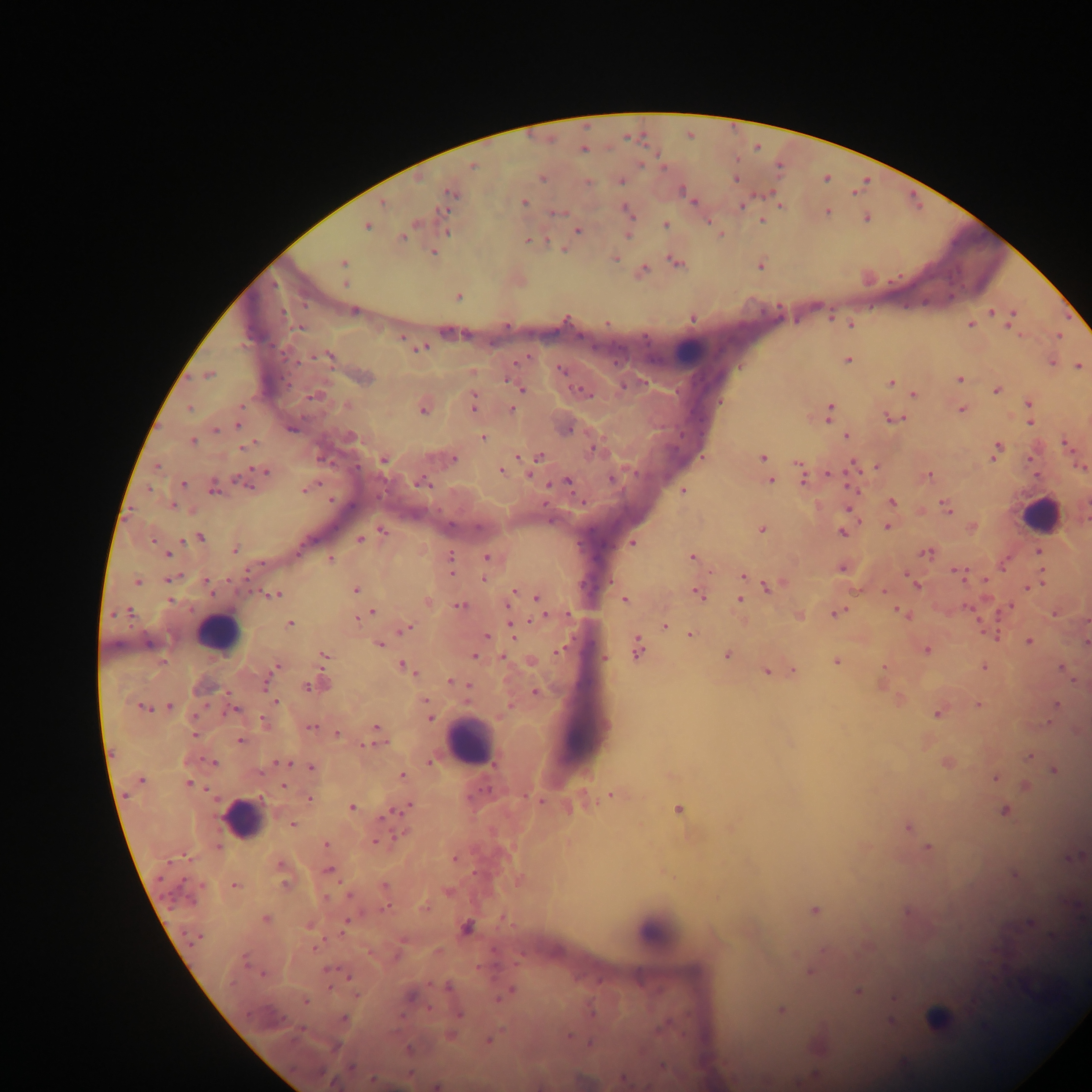
Approximate centers as [x, y] in pixels. Leukocyte locations: [692, 350], [1040, 516], [219, 634], [468, 742], [242, 819], [657, 936]. Malaria parasite locations: [583, 150], [472, 165], [543, 178], [735, 179], [620, 182], [588, 183], [450, 193], [383, 203], [524, 203], [742, 204], [780, 205], [627, 210], [557, 212], [827, 212], [867, 218], [761, 221], [415, 224], [665, 225], [367, 226], [447, 230], [578, 230], [627, 236], [403, 237], [528, 240], [434, 252], [615, 258], [343, 263], [676, 264], [760, 265], [644, 269], [346, 283], [459, 296], [353, 311], [991, 312], [1013, 315], [692, 318], [607, 322], [850, 324], [971, 324], [299, 328], [401, 337], [421, 348], [329, 356], [847, 360], [520, 361], [1051, 362], [1078, 366], [561, 369], [209, 375], [365, 378], [960, 379], [891, 382], [521, 388], [997, 390], [582, 392], [914, 394], [315, 396], [473, 403], [1029, 405], [190, 409], [512, 410], [961, 410], [423, 411], [830, 411], [894, 418], [1030, 423], [238, 425], [292, 428], [216, 430], [568, 430], [846, 436], [352, 437], [483, 438], [192, 441], [1066, 444], [246, 446], [996, 449], [594, 450], [762, 457], [454, 458], [538, 458], [384, 460], [799, 464], [158, 466], [875, 466], [853, 467], [1082, 467], [264, 471], [501, 471], [929, 475], [802, 477], [611, 478], [771, 481], [242, 482], [559, 482], [567, 482], [421, 483], [182, 484], [306, 490], [684, 490], [214, 491], [892, 502], [172, 505], [946, 508], [887, 526], [762, 530], [384, 531], [842, 532], [200, 537], [360, 539], [632, 543], [301, 549], [234, 550], [1038, 552], [167, 554], [927, 554], [692, 557], [450, 558], [487, 558], [331, 560], [1004, 563], [842, 568], [960, 574], [743, 576], [484, 578], [169, 579], [137, 581], [985, 581], [207, 582], [915, 584], [769, 587], [1030, 587], [356, 590], [276, 594], [698, 594], [536, 597], [511, 598], [170, 600], [624, 600], [740, 600], [427, 601], [508, 605], [460, 606], [1010, 607], [372, 612], [129, 613], [837, 613], [901, 613], [1053, 614], [799, 616], [542, 617], [289, 624], [665, 626], [408, 627], [513, 627], [690, 635], [991, 635], [486, 636], [1029, 641], [147, 643], [1086, 643], [379, 644], [561, 649], [637, 649], [927, 649], [324, 656], [475, 656], [727, 656], [503, 657], [604, 657], [836, 662], [276, 666], [403, 667], [884, 668], [983, 668], [1061, 668], [272, 670], [766, 671], [794, 671], [450, 681], [266, 683], [323, 684], [308, 687], [536, 692], [275, 701], [978, 704], [1056, 704], [170, 706], [144, 709], [235, 710], [938, 714], [429, 717], [263, 721], [377, 727], [311, 728], [336, 732], [194, 734], [240, 741], [368, 744], [376, 744], [1028, 757], [430, 762], [214, 763], [282, 763], [947, 763], [311, 767], [1054, 771], [402, 776], [996, 778], [141, 780], [188, 784], [283, 785], [612, 795], [309, 799], [539, 800], [353, 807], [408, 807], [679, 809], [1005, 811], [392, 813], [385, 816], [292, 825], [907, 827], [375, 841], [327, 845], [928, 847], [219, 848], [1073, 857], [186, 858], [455, 858], [328, 870], [1014, 874], [284, 883], [235, 886], [384, 886], [326, 898], [384, 909], [815, 910], [265, 920], [1029, 923], [346, 924], [466, 927], [1053, 936], [195, 938], [314, 948], [245, 960], [328, 970], [810, 971], [262, 974], [348, 975], [448, 987], [510, 991], [858, 992], [355, 994], [410, 997], [499, 999], [306, 1002], [781, 1010], [460, 1015], [343, 1019], [938, 1019], [892, 1021], [568, 1036], [489, 1040], [590, 1043], [409, 1049], [661, 1066], [351, 1067], [321, 1072], [623, 1079], [373, 1080], [436, 1086]. Thick blood film. Sample from Ghana. Single field of view. Mobile-phone photograph taken through the microscope. Image is 1092×1092 pixels.